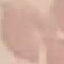
Result: no malaria parasites seen. Photographed with a smartphone camera at the microscope eyepiece. Giemsa-stained preparation. Cell patch, automatically extracted from a larger field of view and resized to 64 × 64 pixels. Thin blood film.